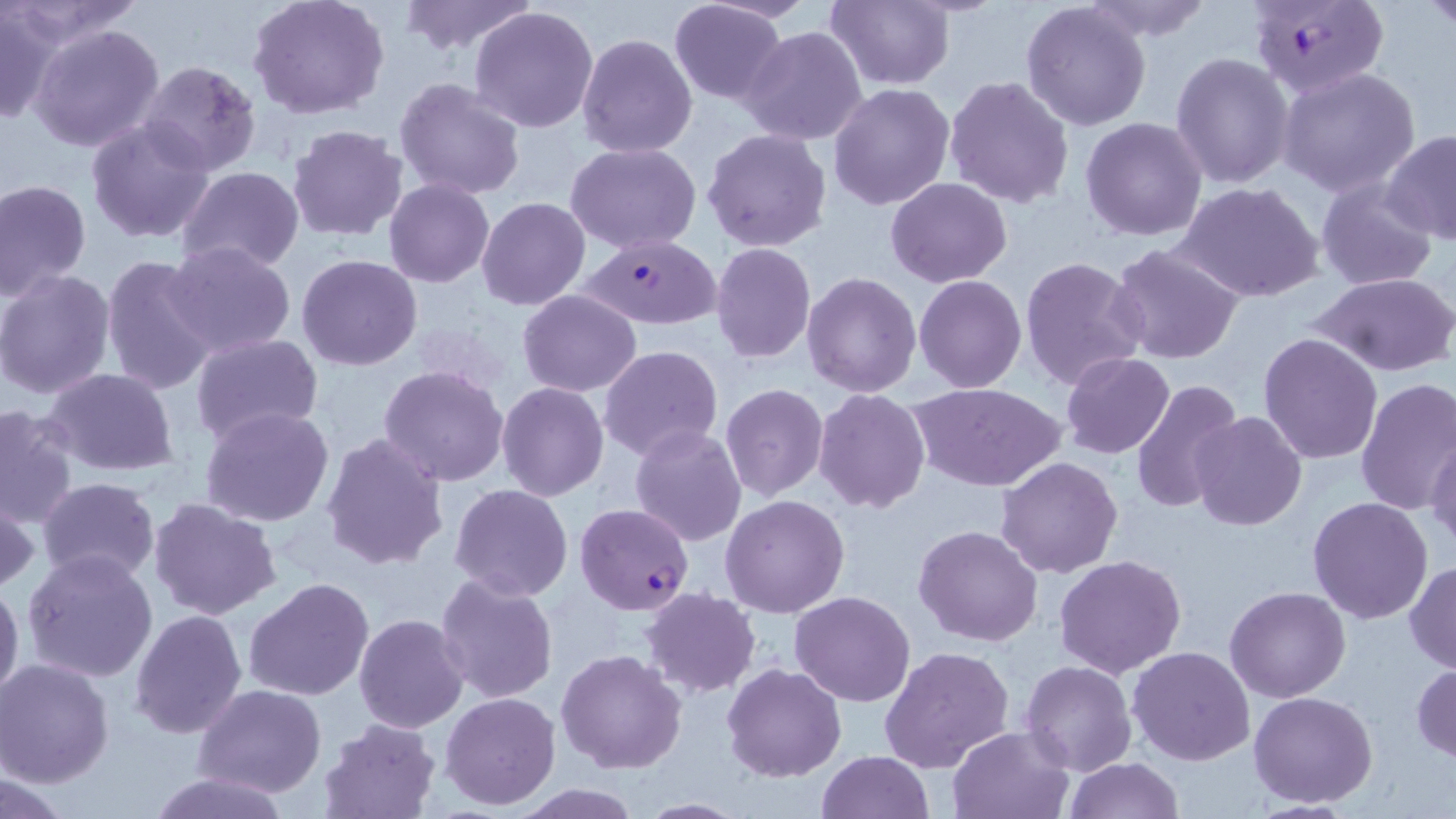 Approximate bounding boxes as named x1/y1/x2/y2 corners in pixels. Uninfected red blood cell locations: (x1=5, y1=0, x2=147, y2=47), (x1=247, y1=0, x2=390, y2=120), (x1=825, y1=0, x2=955, y2=90), (x1=1076, y1=0, x2=1217, y2=42), (x1=1425, y1=0, x2=1454, y2=35), (x1=395, y1=1, x2=538, y2=56), (x1=669, y1=1, x2=789, y2=105), (x1=1021, y1=2, x2=1153, y2=133), (x1=0, y1=6, x2=63, y2=125), (x1=469, y1=6, x2=599, y2=132), (x1=28, y1=22, x2=168, y2=153), (x1=738, y1=25, x2=869, y2=146), (x1=576, y1=32, x2=699, y2=158), (x1=424, y1=33, x2=587, y2=177), (x1=1171, y1=52, x2=1295, y2=191), (x1=138, y1=61, x2=261, y2=175), (x1=1277, y1=67, x2=1420, y2=196), (x1=944, y1=77, x2=1075, y2=208), (x1=394, y1=78, x2=527, y2=202), (x1=827, y1=82, x2=955, y2=211), (x1=85, y1=115, x2=217, y2=244), (x1=1080, y1=117, x2=1207, y2=242), (x1=287, y1=123, x2=408, y2=241), (x1=701, y1=127, x2=832, y2=252), (x1=1381, y1=129, x2=1456, y2=244), (x1=566, y1=142, x2=700, y2=253), (x1=177, y1=166, x2=304, y2=274), (x1=886, y1=177, x2=1012, y2=288), (x1=1316, y1=177, x2=1437, y2=291), (x1=0, y1=178, x2=92, y2=300), (x1=385, y1=180, x2=494, y2=287), (x1=1176, y1=181, x2=1323, y2=304), (x1=477, y1=196, x2=590, y2=310), (x1=163, y1=240, x2=296, y2=358), (x1=1108, y1=243, x2=1246, y2=367), (x1=710, y1=244, x2=816, y2=364), (x1=99, y1=253, x2=220, y2=399), (x1=295, y1=256, x2=422, y2=372), (x1=1018, y1=256, x2=1148, y2=392), (x1=0, y1=270, x2=116, y2=399), (x1=803, y1=272, x2=922, y2=397), (x1=1311, y1=272, x2=1456, y2=378), (x1=915, y1=275, x2=1026, y2=392), (x1=517, y1=289, x2=642, y2=396), (x1=1258, y1=332, x2=1383, y2=464), (x1=190, y1=333, x2=325, y2=446), (x1=599, y1=344, x2=724, y2=462), (x1=1061, y1=353, x2=1174, y2=457), (x1=379, y1=365, x2=509, y2=485), (x1=41, y1=369, x2=181, y2=478), (x1=1131, y1=378, x2=1243, y2=514), (x1=1354, y1=378, x2=1456, y2=518), (x1=911, y1=381, x2=1065, y2=493), (x1=497, y1=382, x2=609, y2=501), (x1=719, y1=383, x2=829, y2=500), (x1=812, y1=389, x2=930, y2=513), (x1=0, y1=404, x2=79, y2=530), (x1=200, y1=406, x2=335, y2=528), (x1=1189, y1=412, x2=1307, y2=531), (x1=629, y1=425, x2=747, y2=547), (x1=320, y1=432, x2=450, y2=571), (x1=1427, y1=434, x2=1456, y2=552), (x1=995, y1=455, x2=1123, y2=578), (x1=36, y1=478, x2=161, y2=588), (x1=450, y1=484, x2=572, y2=601), (x1=721, y1=494, x2=849, y2=617), (x1=148, y1=496, x2=282, y2=623), (x1=1, y1=497, x2=38, y2=595), (x1=1307, y1=497, x2=1434, y2=624), (x1=913, y1=524, x2=1042, y2=647), (x1=21, y1=549, x2=160, y2=683), (x1=1054, y1=554, x2=1187, y2=677), (x1=1405, y1=560, x2=1456, y2=673), (x1=434, y1=571, x2=561, y2=705), (x1=244, y1=576, x2=374, y2=701), (x1=0, y1=578, x2=24, y2=709), (x1=1225, y1=585, x2=1350, y2=702), (x1=642, y1=588, x2=761, y2=697), (x1=790, y1=591, x2=915, y2=706), (x1=129, y1=609, x2=247, y2=738), (x1=353, y1=613, x2=469, y2=733), (x1=880, y1=645, x2=1014, y2=775), (x1=1127, y1=646, x2=1256, y2=767), (x1=556, y1=649, x2=688, y2=774), (x1=0, y1=659, x2=117, y2=789), (x1=1021, y1=660, x2=1136, y2=776), (x1=1410, y1=662, x2=1456, y2=763), (x1=723, y1=663, x2=848, y2=783), (x1=195, y1=684, x2=328, y2=798), (x1=441, y1=691, x2=561, y2=809), (x1=1248, y1=691, x2=1379, y2=808), (x1=320, y1=717, x2=438, y2=818), (x1=947, y1=724, x2=1074, y2=817), (x1=815, y1=751, x2=934, y2=818), (x1=1063, y1=756, x2=1185, y2=818), (x1=149, y1=769, x2=293, y2=818), (x1=1, y1=773, x2=78, y2=818), (x1=511, y1=783, x2=641, y2=818), (x1=630, y1=798, x2=749, y2=817). Plasmodium falciparum-infected red blood cell locations: (x1=1249, y1=0, x2=1388, y2=99), (x1=578, y1=233, x2=724, y2=329), (x1=575, y1=503, x2=694, y2=614). Slide-level diagnosis: Plasmodium falciparum. Thin blood film. Single field of view. May-Grünwald-Giemsa-stained preparation. Optical microscopy. Image is 1456×819 pixels. 1000x magnification.